Give a bounding box for every parasitised red blood cell, every trophozoite, every gametocyte, every leukocyte, and every artifact (platelet-like body, stain precipitate, or debris).
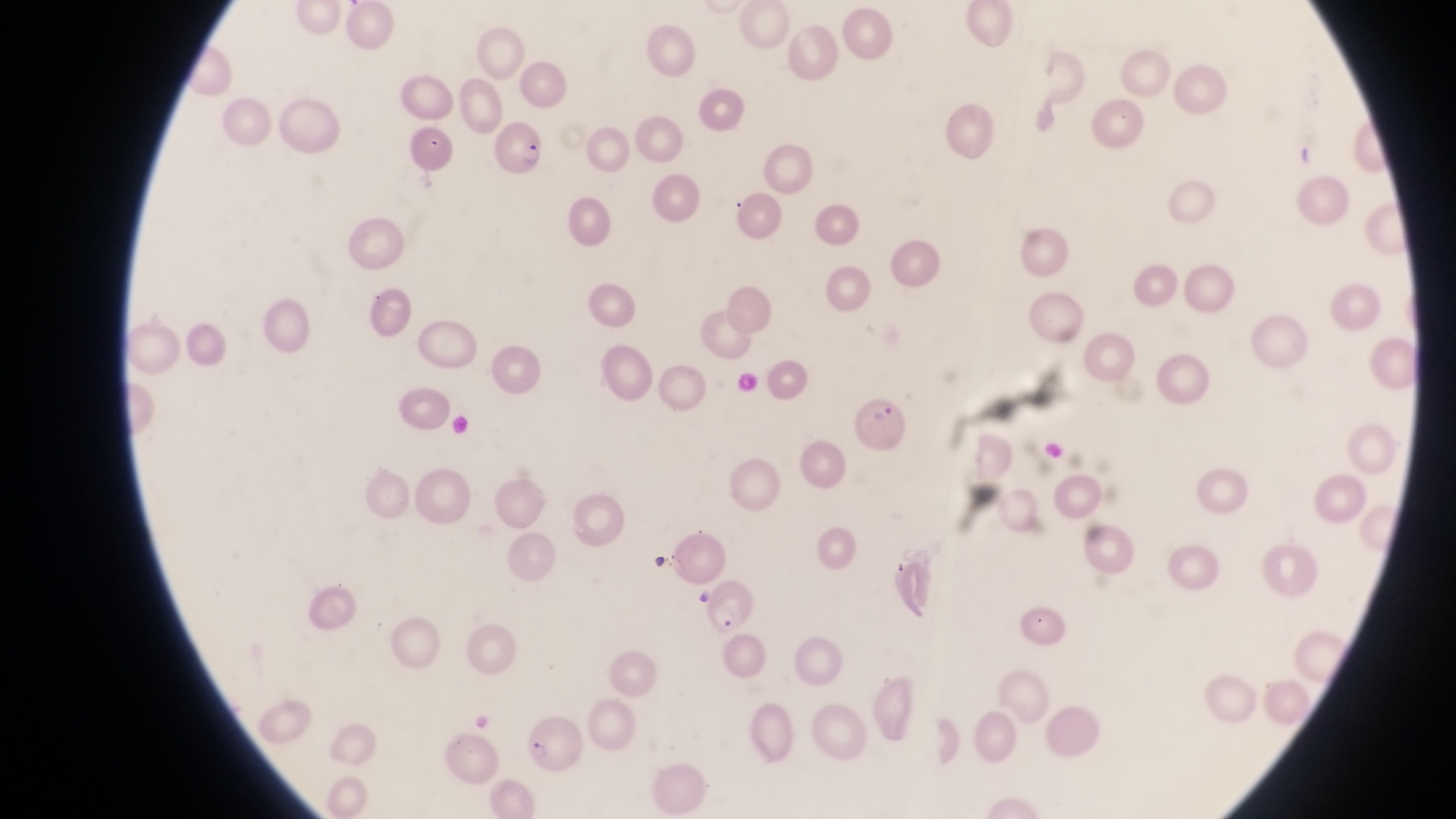

Approximate bounding boxes as [left, top, right, bottom] in pixels.
Parasitised red blood cells: [491, 121, 552, 177], [855, 391, 910, 455], [704, 578, 765, 638], [518, 710, 590, 777].
No leukocytes observed.

Summary:
  - Preparation: thin blood smear
  - Magnification: 1000x
  - Capture: smartphone photograph through the eyepiece of an Olympus CX-23 microscope
  - Country: Uganda
  - Field of view: single
  - Image size: 1456×819 pixels